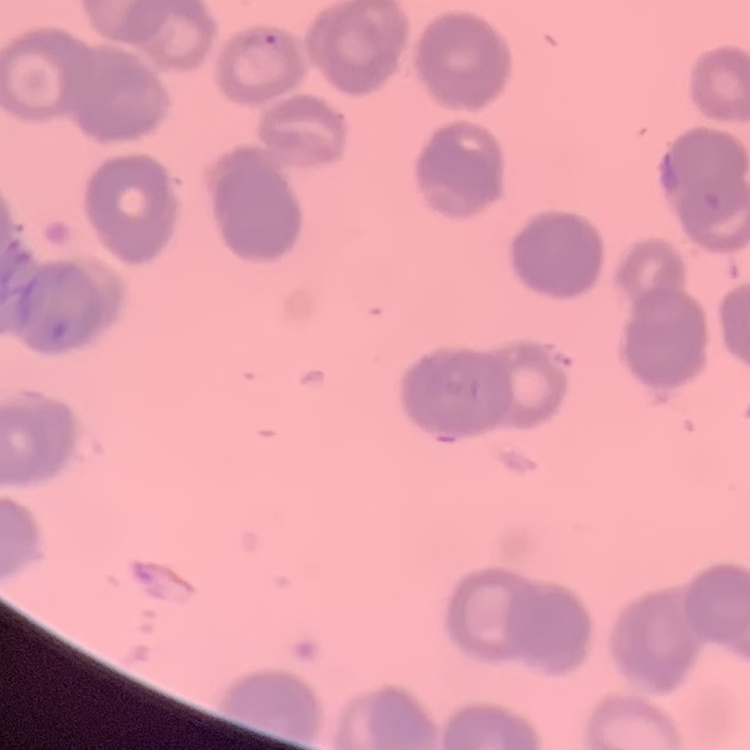

Summary:
  - Red blood cell morphology: rouleaux formation
  - Image type: one tile cut from a larger photomicrograph
  - Stain: Field's or Giemsa
  - Preparation: thin peripheral smear